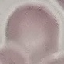
Result: no malaria parasites seen. Thin smear of blood. Photographed with a smartphone camera at the microscope eyepiece. Giemsa stain. Automatically extracted cell patch, resized to 64 × 64 pixels.